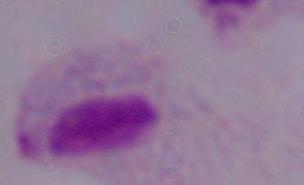
{
  "magnification": "1000x",
  "identification": "trichomonad",
  "modality": "micrograph"
}